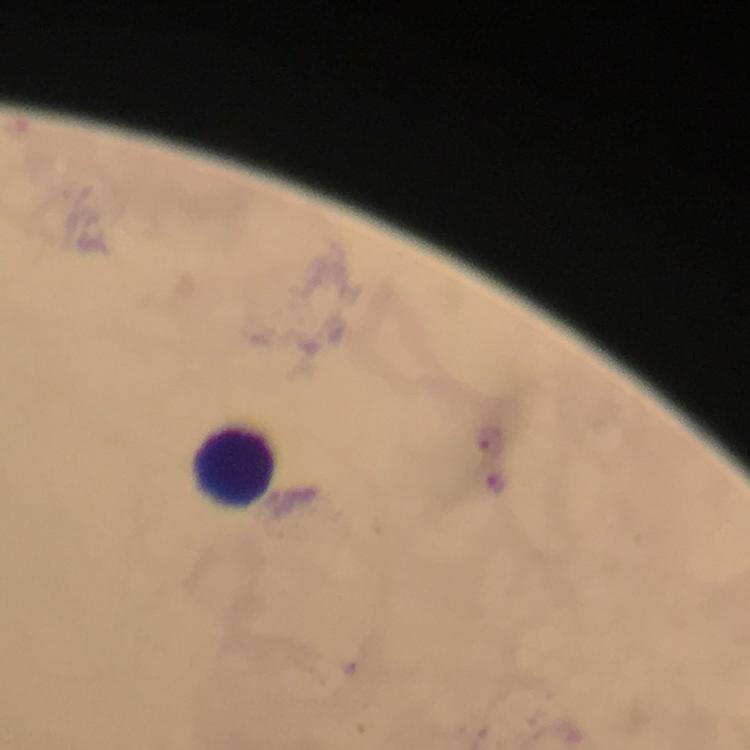
cropped from = a single field of view
stain = Giemsa
magnification = 100x
capture = smartphone mounted on the microscope
malaria parasite locations = approximate centers as [x, y] in pixels: [488, 444], [495, 479]
context = from a diagnostic examination for malaria
immersion oil = used
preparation = thick smear
image size = 750×750 pixels
leukocyte locations = approximate centers as [x, y] in pixels: [234, 464]